Report the malaria status of this cell.
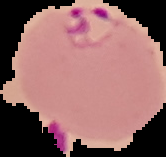

It is parasitized.

From a thin blood film. Image is 166×157 pixels. Segmented cell region on a black background.